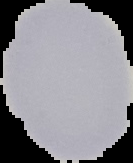

{
  "image_type": "segmented cell region on a black background",
  "result": "no malaria parasites detected",
  "preparation": "thin blood smear",
  "image_size": "133×163 pixels"
}